Name the blood parasite species.
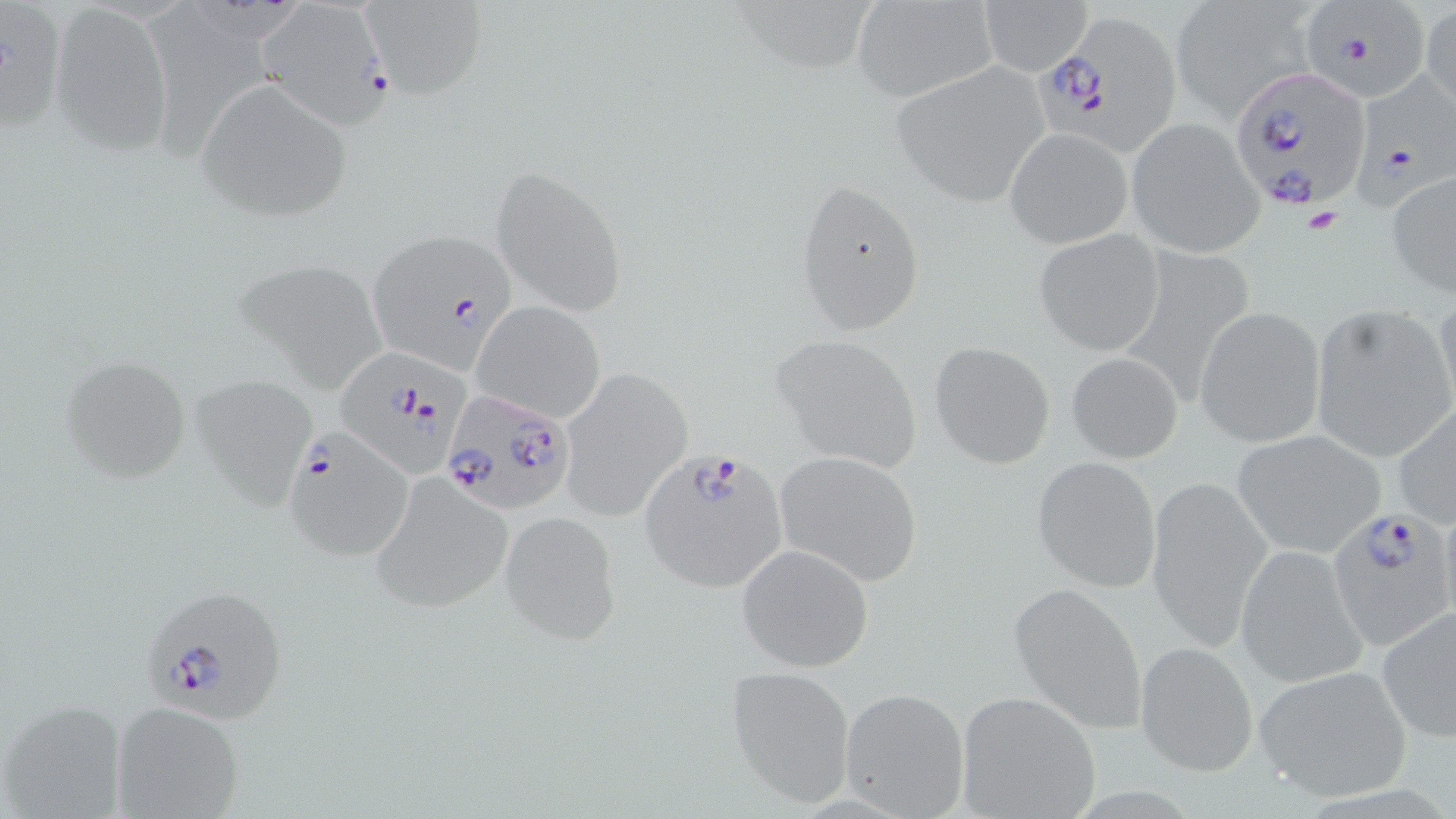

Plasmodium falciparum.

modality = light microscopy
Plasmodium falciparum-infected red blood cell locations = approximate bounding boxes as named x1/y1/x2/y2 corners in pixels: (x1=257, y1=2, x2=391, y2=123), (x1=1299, y1=6, x2=1433, y2=105), (x1=1032, y1=11, x2=1184, y2=155), (x1=1227, y1=67, x2=1372, y2=214), (x1=1354, y1=76, x2=1455, y2=217), (x1=365, y1=231, x2=519, y2=372), (x1=336, y1=349, x2=472, y2=478), (x1=441, y1=389, x2=573, y2=516), (x1=285, y1=428, x2=412, y2=561), (x1=640, y1=447, x2=792, y2=595), (x1=1334, y1=500, x2=1456, y2=643), (x1=146, y1=584, x2=290, y2=731)
field of view = single
preparation = thin blood film
magnification = 1000x
stain = May-Grünwald-Giemsa
platelet locations = approximate bounding boxes as named x1/y1/x2/y2 corners in pixels: (x1=1302, y1=208, x2=1345, y2=235)
uninfected red blood cell locations = approximate bounding boxes as named x1/y1/x2/y2 corners in pixels: (x1=360, y1=0, x2=487, y2=99), (x1=850, y1=0, x2=1000, y2=103), (x1=978, y1=0, x2=1093, y2=76), (x1=1169, y1=0, x2=1318, y2=123), (x1=1420, y1=3, x2=1456, y2=116), (x1=49, y1=5, x2=173, y2=156), (x1=890, y1=65, x2=1049, y2=204), (x1=194, y1=80, x2=354, y2=223), (x1=1124, y1=117, x2=1266, y2=257), (x1=1005, y1=128, x2=1132, y2=247), (x1=490, y1=163, x2=628, y2=318), (x1=1385, y1=171, x2=1456, y2=298), (x1=794, y1=176, x2=926, y2=337), (x1=1034, y1=228, x2=1165, y2=356), (x1=227, y1=258, x2=392, y2=394), (x1=1432, y1=293, x2=1456, y2=424), (x1=472, y1=302, x2=606, y2=425), (x1=1308, y1=304, x2=1456, y2=463), (x1=1194, y1=306, x2=1327, y2=449), (x1=770, y1=333, x2=924, y2=472), (x1=929, y1=342, x2=1056, y2=468), (x1=1065, y1=352, x2=1183, y2=464), (x1=60, y1=353, x2=193, y2=483), (x1=560, y1=366, x2=694, y2=522), (x1=190, y1=372, x2=320, y2=510), (x1=1391, y1=403, x2=1456, y2=528), (x1=1232, y1=430, x2=1387, y2=559), (x1=776, y1=452, x2=923, y2=586), (x1=1032, y1=456, x2=1161, y2=592), (x1=370, y1=474, x2=512, y2=614), (x1=1143, y1=474, x2=1272, y2=653), (x1=502, y1=511, x2=621, y2=643), (x1=736, y1=544, x2=874, y2=673), (x1=1234, y1=546, x2=1367, y2=687), (x1=1008, y1=582, x2=1147, y2=733), (x1=1377, y1=604, x2=1456, y2=744), (x1=1135, y1=641, x2=1257, y2=777), (x1=725, y1=664, x2=856, y2=808), (x1=1253, y1=665, x2=1414, y2=803), (x1=838, y1=686, x2=971, y2=819), (x1=954, y1=690, x2=1102, y2=819), (x1=0, y1=698, x2=129, y2=819), (x1=110, y1=700, x2=246, y2=819)
image size = 1456×819 pixels